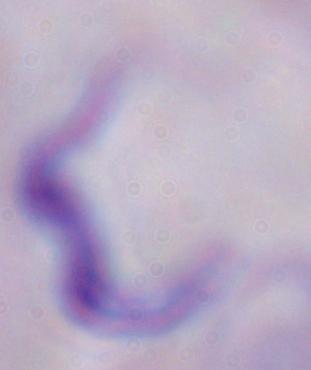

magnification = 1000x
identification = trypanosome
modality = micrograph